Name the parasite shown.
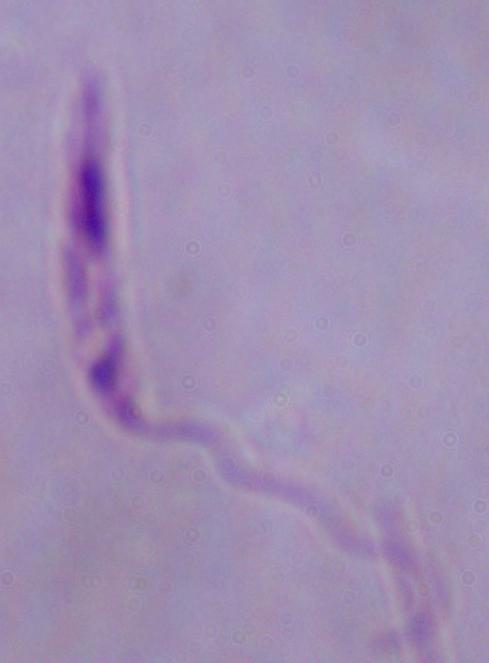
This is Leishmania.

{
  "magnification": "1000x",
  "modality": "micrograph"
}